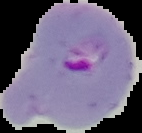
image size = 142×133 pixels
image type = cell region segmented out of the field of view; surrounding area masked to black
preparation = thin blood film
malaria status = parasitized